State which parasite is depicted.
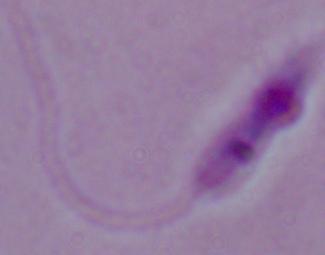

Leishmania.

Summary:
  - Modality: micrograph
  - Magnification: 1000x